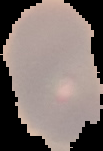
Summary:
  - Result: no Plasmodium parasites detected
  - Image type: segmented cell region on a black background
  - Image size: 103×151 pixels
  - Preparation: thin blood film